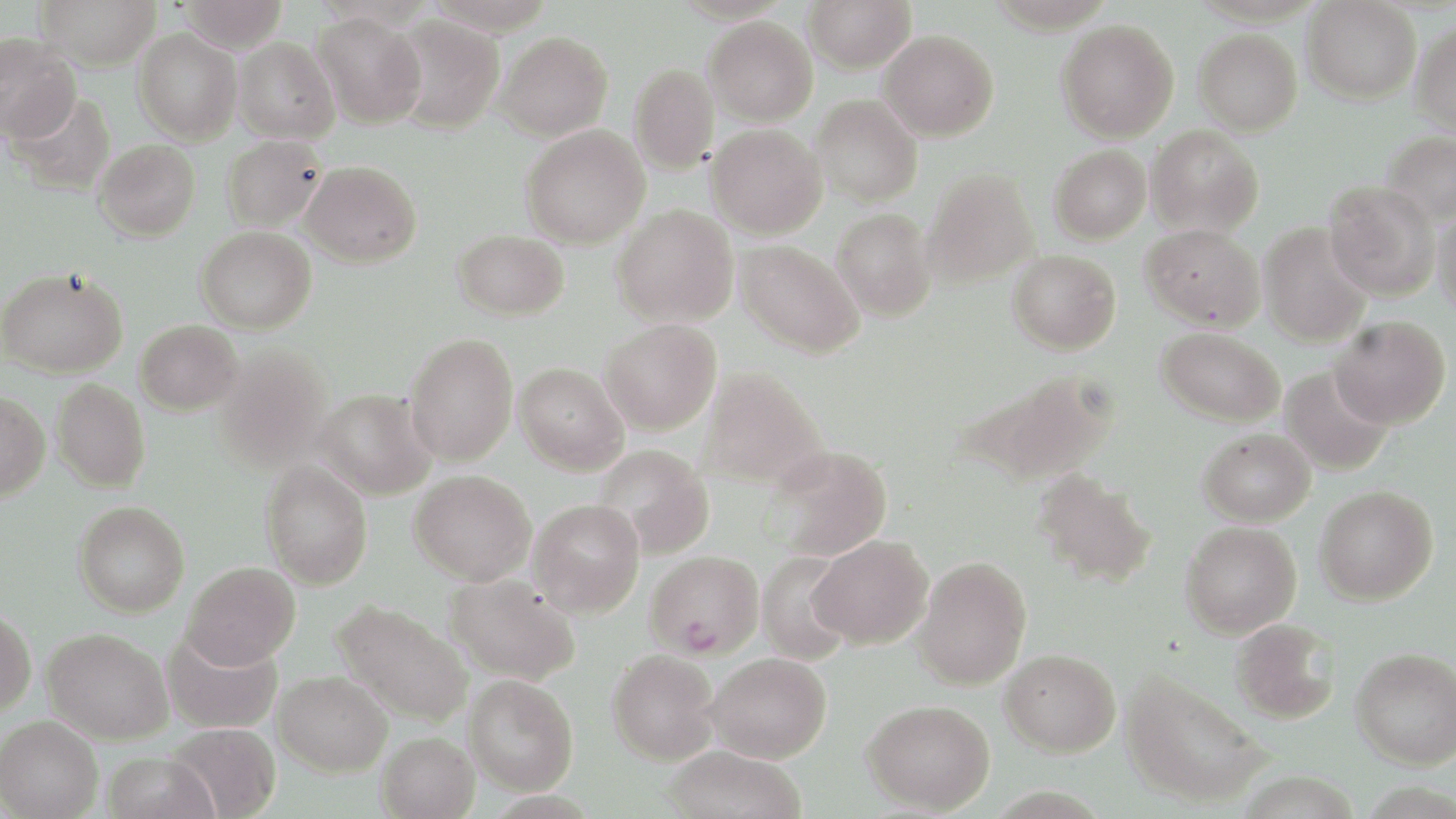
Summary:
  - Coordinate format: approximate bounding boxes as named x1/y1/x2/y2 corners in pixels
  - Plasmodium falciparum-infected red blood cell locations: (x1=646, y1=550, x2=764, y2=659)
  - Uninfected red blood cell locations: (x1=37, y1=0, x2=161, y2=70), (x1=180, y1=0, x2=288, y2=53), (x1=804, y1=0, x2=916, y2=73), (x1=1303, y1=0, x2=1420, y2=104), (x1=313, y1=11, x2=427, y2=129), (x1=389, y1=15, x2=505, y2=133), (x1=704, y1=16, x2=817, y2=125), (x1=1056, y1=20, x2=1180, y2=143), (x1=1411, y1=23, x2=1456, y2=134), (x1=133, y1=29, x2=242, y2=144), (x1=1194, y1=29, x2=1302, y2=136), (x1=879, y1=30, x2=999, y2=141), (x1=494, y1=32, x2=613, y2=141), (x1=0, y1=34, x2=80, y2=143), (x1=234, y1=37, x2=339, y2=144), (x1=629, y1=63, x2=719, y2=174), (x1=7, y1=90, x2=117, y2=197), (x1=811, y1=95, x2=922, y2=207), (x1=520, y1=124, x2=650, y2=249), (x1=706, y1=124, x2=827, y2=240), (x1=1146, y1=125, x2=1264, y2=237), (x1=1381, y1=130, x2=1456, y2=227), (x1=221, y1=135, x2=327, y2=231), (x1=93, y1=139, x2=200, y2=241), (x1=1048, y1=145, x2=1151, y2=245), (x1=300, y1=160, x2=422, y2=268), (x1=921, y1=169, x2=1039, y2=289), (x1=1324, y1=180, x2=1441, y2=301), (x1=1433, y1=204, x2=1456, y2=318), (x1=612, y1=205, x2=738, y2=328), (x1=831, y1=208, x2=937, y2=322), (x1=1140, y1=223, x2=1265, y2=332), (x1=1259, y1=224, x2=1373, y2=347), (x1=196, y1=225, x2=317, y2=333), (x1=452, y1=229, x2=570, y2=321), (x1=735, y1=240, x2=865, y2=358), (x1=1007, y1=249, x2=1121, y2=355), (x1=1, y1=266, x2=128, y2=378), (x1=1330, y1=316, x2=1451, y2=429), (x1=135, y1=319, x2=242, y2=414), (x1=599, y1=320, x2=721, y2=435), (x1=1157, y1=327, x2=1285, y2=426), (x1=405, y1=332, x2=518, y2=466), (x1=214, y1=343, x2=333, y2=470), (x1=515, y1=362, x2=628, y2=474), (x1=1280, y1=365, x2=1394, y2=476), (x1=697, y1=366, x2=829, y2=491), (x1=955, y1=367, x2=1117, y2=488), (x1=52, y1=379, x2=150, y2=493), (x1=314, y1=388, x2=436, y2=500), (x1=0, y1=390, x2=50, y2=500), (x1=1198, y1=428, x2=1315, y2=526), (x1=593, y1=444, x2=714, y2=559), (x1=765, y1=446, x2=893, y2=561), (x1=260, y1=460, x2=373, y2=589), (x1=1030, y1=468, x2=1158, y2=589), (x1=409, y1=469, x2=536, y2=585), (x1=1314, y1=485, x2=1439, y2=605), (x1=529, y1=499, x2=645, y2=617), (x1=74, y1=501, x2=190, y2=617), (x1=1180, y1=521, x2=1301, y2=639), (x1=808, y1=535, x2=933, y2=648), (x1=756, y1=550, x2=857, y2=665), (x1=913, y1=556, x2=1032, y2=690), (x1=182, y1=561, x2=301, y2=669), (x1=445, y1=574, x2=581, y2=684), (x1=331, y1=599, x2=474, y2=727), (x1=0, y1=606, x2=37, y2=716), (x1=1229, y1=618, x2=1341, y2=725), (x1=42, y1=627, x2=173, y2=744), (x1=162, y1=629, x2=282, y2=733), (x1=1351, y1=646, x2=1455, y2=769), (x1=1000, y1=648, x2=1121, y2=757), (x1=607, y1=649, x2=720, y2=765), (x1=705, y1=651, x2=833, y2=763), (x1=273, y1=670, x2=392, y2=776), (x1=1120, y1=670, x2=1270, y2=809), (x1=464, y1=675, x2=578, y2=794), (x1=862, y1=699, x2=995, y2=814), (x1=0, y1=715, x2=103, y2=819), (x1=166, y1=722, x2=282, y2=819), (x1=376, y1=731, x2=480, y2=819), (x1=661, y1=744, x2=807, y2=819), (x1=101, y1=751, x2=219, y2=819)
  - Slide-level diagnosis: Plasmodium falciparum
  - Image size: 1456×819 pixels
  - Modality: optical microscopy
  - Magnification: 1000x
  - Stain: May-Grünwald-Giemsa
  - Preparation: thin blood film
  - Field of view: one of a larger specimen